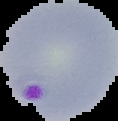

Summary:
  - Image type: cell region segmented out of the field of view; surrounding area masked to black
  - Image size: 118×121 pixels
  - Result: malaria parasites identified
  - Preparation: thin blood smear